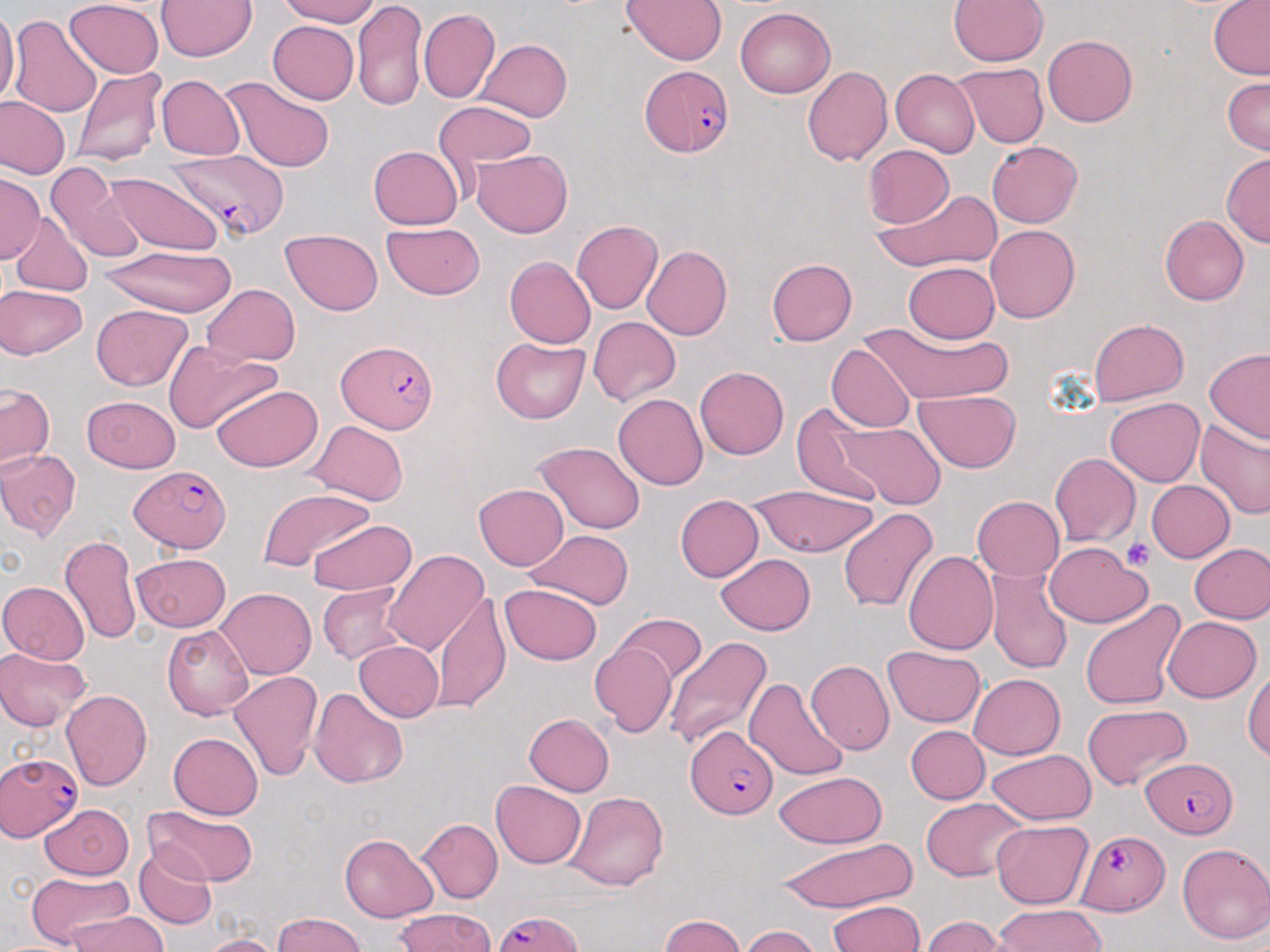

Approximate bounding boxes as (x1, y1, x2, y2) in pixels. Uninfected red blood cell locations: (159, 0, 256, 62), (274, 0, 385, 26), (623, 0, 728, 64), (950, 0, 1048, 67), (1206, 0, 1270, 79), (66, 1, 163, 77), (352, 1, 429, 114), (736, 7, 836, 99), (420, 9, 500, 104), (0, 10, 17, 109), (10, 14, 102, 115), (266, 18, 356, 103), (1042, 33, 1137, 125), (476, 40, 572, 122), (952, 63, 1051, 149), (72, 65, 165, 168), (802, 66, 891, 167), (891, 69, 978, 155), (156, 75, 243, 159), (221, 76, 338, 173), (1220, 76, 1269, 155), (2, 98, 69, 179), (432, 104, 537, 173), (987, 140, 1085, 227), (368, 146, 463, 230), (862, 146, 955, 229), (471, 149, 573, 237), (1221, 154, 1269, 248), (51, 170, 150, 263), (109, 172, 221, 253), (0, 175, 42, 267), (868, 186, 1004, 273), (1161, 214, 1251, 306), (11, 219, 93, 299), (571, 220, 661, 314), (383, 223, 485, 298), (986, 224, 1081, 323), (280, 229, 384, 314), (98, 243, 238, 316), (643, 245, 733, 339), (504, 256, 595, 348), (767, 259, 857, 345), (904, 262, 998, 342), (200, 283, 300, 366), (0, 284, 88, 360), (91, 305, 195, 391), (587, 316, 680, 406), (1087, 318, 1188, 404), (857, 322, 1016, 403), (490, 336, 590, 424), (828, 343, 916, 432), (163, 345, 279, 433), (1203, 348, 1270, 443), (695, 367, 789, 459), (0, 384, 55, 469), (210, 384, 323, 472), (915, 391, 1023, 472), (613, 393, 706, 490), (84, 395, 183, 470), (1105, 397, 1204, 488), (792, 402, 888, 503), (1194, 417, 1270, 522), (308, 420, 405, 504), (834, 420, 947, 507), (533, 441, 646, 534), (0, 446, 81, 539), (1048, 452, 1138, 547), (1146, 481, 1235, 563), (474, 483, 569, 571), (256, 485, 377, 573), (743, 489, 882, 558), (675, 494, 764, 581), (973, 495, 1065, 583), (837, 508, 939, 614), (305, 519, 417, 597), (523, 529, 632, 609), (58, 535, 141, 647), (1188, 542, 1270, 626), (1045, 544, 1152, 627), (900, 548, 999, 658), (384, 549, 488, 658), (130, 553, 232, 632), (716, 553, 816, 636), (989, 571, 1073, 675), (0, 580, 90, 666), (502, 580, 601, 663), (317, 585, 413, 666), (216, 589, 315, 678), (430, 595, 509, 711), (1078, 598, 1186, 712), (614, 614, 706, 685), (1163, 615, 1261, 702), (163, 625, 255, 720), (665, 636, 772, 752), (353, 641, 443, 721), (885, 643, 987, 728), (589, 644, 677, 737), (0, 646, 93, 732), (806, 659, 893, 755), (1244, 665, 1269, 764), (225, 668, 321, 780), (967, 674, 1066, 759), (747, 676, 848, 779), (309, 685, 408, 791), (61, 688, 152, 792), (1082, 706, 1190, 790), (522, 713, 614, 796), (906, 726, 988, 804), (168, 733, 262, 820), (984, 747, 1093, 824), (771, 771, 888, 846), (490, 781, 587, 866), (563, 791, 669, 891), (920, 797, 1028, 882), (141, 802, 259, 889), (37, 803, 136, 879), (418, 819, 504, 901), (992, 820, 1093, 907), (339, 834, 438, 921), (774, 839, 918, 912), (1175, 840, 1270, 946), (134, 847, 217, 930), (22, 870, 137, 946), (828, 898, 925, 952), (992, 903, 1110, 952), (391, 909, 499, 952), (65, 913, 172, 952), (271, 913, 369, 952), (921, 913, 1006, 952), (657, 914, 752, 952), (739, 925, 822, 952), (200, 933, 283, 952). Plasmodium falciparum-infected red blood cell locations: (641, 69, 736, 159), (163, 151, 286, 238), (335, 338, 439, 434), (129, 464, 232, 553), (687, 727, 777, 820), (0, 751, 87, 841), (1140, 755, 1239, 836), (1071, 831, 1168, 914), (487, 908, 587, 952). Platelet locations: (1125, 537, 1155, 571). Slide-level diagnosis: Plasmodium falciparum. Captured at 1000x magnification. Image is 1270×952 pixels. May-Grünwald-Giemsa stain. One field of a larger specimen. Thin blood film. Light microscopy.